Identify the blood parasite species.
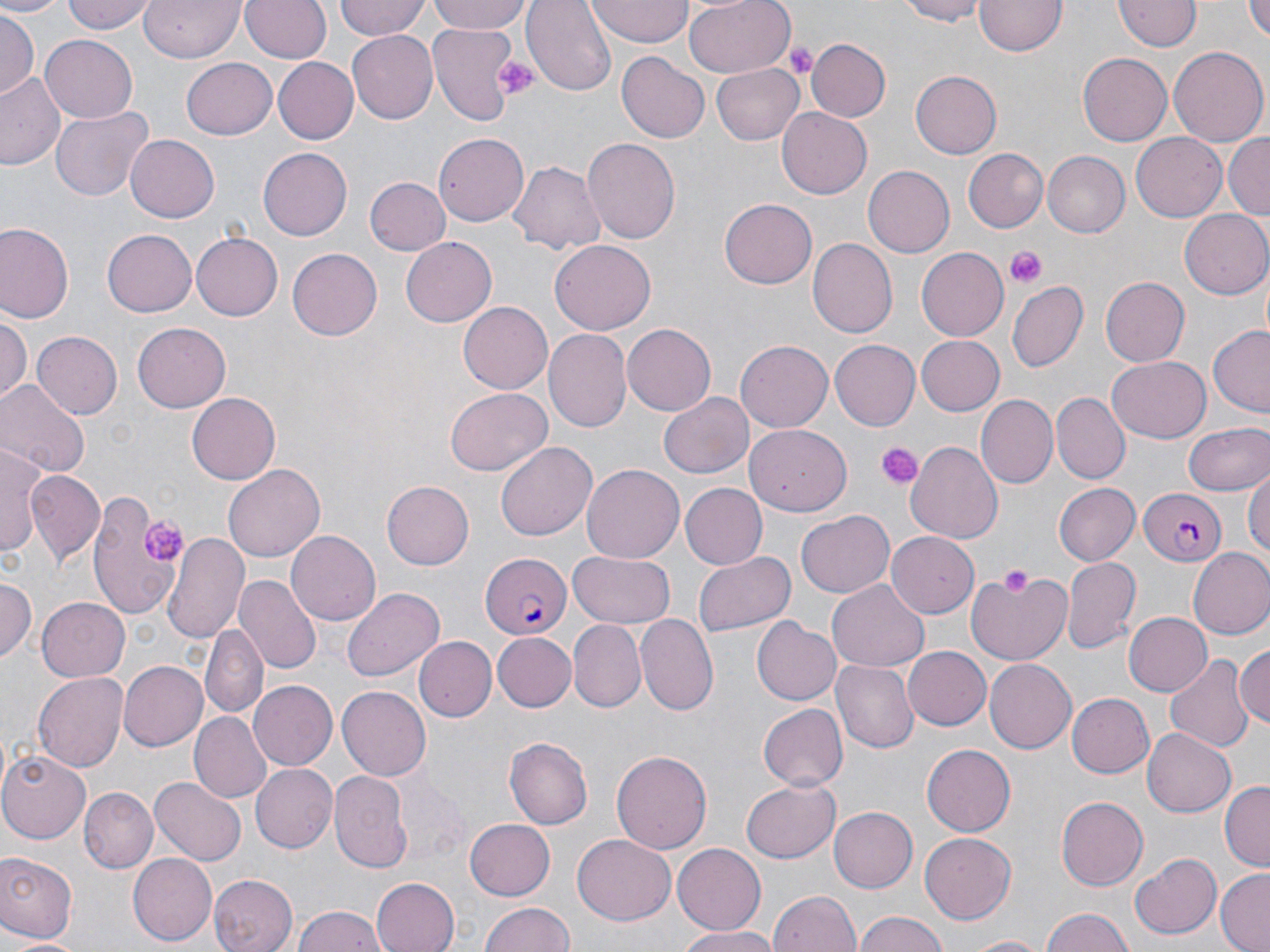

Plasmodium falciparum.

magnification = 1000x
Plasmodium falciparum-infected red blood cell locations = approximate bounding boxes as named x1/y1/x2/y2 corners in pixels: (x1=1137, y1=487, x2=1228, y2=567), (x1=481, y1=554, x2=571, y2=639)
uninfected red blood cell locations = approximate bounding boxes as named x1/y1/x2/y2 corners in pixels: (x1=0, y1=0, x2=61, y2=17), (x1=64, y1=0, x2=156, y2=35), (x1=137, y1=0, x2=246, y2=63), (x1=240, y1=0, x2=333, y2=63), (x1=333, y1=0, x2=431, y2=41), (x1=428, y1=0, x2=534, y2=36), (x1=523, y1=0, x2=617, y2=95), (x1=682, y1=0, x2=796, y2=78), (x1=893, y1=0, x2=992, y2=25), (x1=1117, y1=0, x2=1199, y2=52), (x1=975, y1=1, x2=1065, y2=56), (x1=587, y1=2, x2=697, y2=45), (x1=1245, y1=2, x2=1270, y2=44), (x1=0, y1=11, x2=37, y2=98), (x1=427, y1=21, x2=523, y2=127), (x1=346, y1=30, x2=438, y2=123), (x1=40, y1=33, x2=137, y2=119), (x1=805, y1=38, x2=891, y2=123), (x1=1171, y1=48, x2=1267, y2=145), (x1=616, y1=50, x2=710, y2=142), (x1=1078, y1=51, x2=1174, y2=146), (x1=272, y1=56, x2=359, y2=143), (x1=182, y1=58, x2=277, y2=139), (x1=710, y1=64, x2=805, y2=143), (x1=0, y1=71, x2=65, y2=171), (x1=911, y1=71, x2=1001, y2=158), (x1=50, y1=103, x2=152, y2=202), (x1=776, y1=107, x2=872, y2=199), (x1=435, y1=133, x2=528, y2=229), (x1=1130, y1=133, x2=1227, y2=222), (x1=1225, y1=133, x2=1270, y2=222), (x1=126, y1=135, x2=219, y2=222), (x1=580, y1=135, x2=679, y2=242), (x1=258, y1=148, x2=353, y2=239), (x1=963, y1=148, x2=1050, y2=232), (x1=1042, y1=152, x2=1130, y2=238), (x1=507, y1=160, x2=608, y2=257), (x1=864, y1=165, x2=954, y2=257), (x1=364, y1=175, x2=450, y2=257), (x1=720, y1=199, x2=816, y2=288), (x1=1181, y1=209, x2=1270, y2=298), (x1=0, y1=224, x2=75, y2=325), (x1=102, y1=228, x2=197, y2=317), (x1=192, y1=231, x2=283, y2=321), (x1=401, y1=237, x2=496, y2=327), (x1=549, y1=238, x2=656, y2=334), (x1=806, y1=238, x2=896, y2=337), (x1=915, y1=246, x2=1008, y2=341), (x1=288, y1=247, x2=385, y2=340), (x1=1101, y1=276, x2=1189, y2=367), (x1=1009, y1=280, x2=1087, y2=371), (x1=457, y1=302, x2=553, y2=395), (x1=0, y1=317, x2=29, y2=402), (x1=133, y1=321, x2=231, y2=413), (x1=621, y1=324, x2=716, y2=417), (x1=1208, y1=326, x2=1270, y2=415), (x1=544, y1=329, x2=631, y2=432), (x1=31, y1=332, x2=122, y2=420), (x1=914, y1=335, x2=1004, y2=415), (x1=737, y1=341, x2=832, y2=431), (x1=831, y1=341, x2=920, y2=430), (x1=1107, y1=357, x2=1212, y2=442), (x1=0, y1=380, x2=87, y2=481), (x1=445, y1=387, x2=552, y2=476), (x1=1051, y1=392, x2=1128, y2=484), (x1=186, y1=393, x2=279, y2=484), (x1=661, y1=393, x2=754, y2=478), (x1=977, y1=394, x2=1057, y2=488), (x1=746, y1=421, x2=851, y2=513), (x1=1183, y1=421, x2=1270, y2=497), (x1=495, y1=439, x2=596, y2=538), (x1=906, y1=440, x2=1003, y2=543), (x1=0, y1=442, x2=46, y2=558), (x1=225, y1=463, x2=325, y2=559), (x1=582, y1=464, x2=686, y2=563), (x1=1244, y1=468, x2=1270, y2=564), (x1=28, y1=470, x2=104, y2=564), (x1=382, y1=481, x2=474, y2=568), (x1=678, y1=482, x2=766, y2=569), (x1=1053, y1=484, x2=1141, y2=564), (x1=84, y1=490, x2=179, y2=620), (x1=796, y1=510, x2=895, y2=597), (x1=288, y1=529, x2=383, y2=626), (x1=887, y1=531, x2=979, y2=617), (x1=161, y1=532, x2=249, y2=644), (x1=1187, y1=548, x2=1270, y2=641), (x1=693, y1=549, x2=795, y2=639), (x1=566, y1=551, x2=678, y2=628), (x1=1061, y1=555, x2=1141, y2=653), (x1=965, y1=570, x2=1072, y2=666), (x1=234, y1=576, x2=321, y2=675), (x1=0, y1=577, x2=37, y2=663), (x1=829, y1=579, x2=930, y2=671), (x1=344, y1=587, x2=446, y2=682), (x1=38, y1=598, x2=130, y2=681), (x1=1124, y1=612, x2=1209, y2=695), (x1=634, y1=614, x2=717, y2=715), (x1=752, y1=619, x2=840, y2=706), (x1=570, y1=622, x2=645, y2=711), (x1=203, y1=625, x2=266, y2=722), (x1=493, y1=633, x2=576, y2=712), (x1=414, y1=637, x2=495, y2=722), (x1=1234, y1=644, x2=1269, y2=733), (x1=902, y1=645, x2=991, y2=729), (x1=1166, y1=654, x2=1250, y2=751), (x1=833, y1=658, x2=918, y2=752), (x1=985, y1=658, x2=1078, y2=753), (x1=118, y1=660, x2=209, y2=751), (x1=34, y1=672, x2=130, y2=772), (x1=248, y1=680, x2=337, y2=771), (x1=338, y1=686, x2=432, y2=781), (x1=1065, y1=692, x2=1155, y2=779), (x1=756, y1=703, x2=847, y2=791), (x1=188, y1=712, x2=272, y2=803), (x1=1142, y1=726, x2=1235, y2=816), (x1=504, y1=736, x2=594, y2=830), (x1=921, y1=743, x2=1016, y2=837), (x1=611, y1=749, x2=713, y2=857), (x1=0, y1=754, x2=91, y2=842), (x1=249, y1=763, x2=337, y2=852), (x1=329, y1=771, x2=412, y2=873), (x1=389, y1=772, x2=467, y2=862), (x1=151, y1=776, x2=245, y2=865), (x1=741, y1=780, x2=840, y2=863), (x1=1220, y1=782, x2=1270, y2=870), (x1=79, y1=788, x2=158, y2=873), (x1=1056, y1=795, x2=1148, y2=891), (x1=829, y1=806, x2=917, y2=893), (x1=465, y1=820, x2=557, y2=900), (x1=922, y1=832, x2=1018, y2=924), (x1=573, y1=835, x2=676, y2=923), (x1=673, y1=843, x2=765, y2=934), (x1=128, y1=852, x2=217, y2=944), (x1=1130, y1=852, x2=1222, y2=939), (x1=0, y1=853, x2=77, y2=942), (x1=1214, y1=869, x2=1270, y2=951), (x1=210, y1=873, x2=297, y2=952), (x1=370, y1=876, x2=458, y2=952), (x1=766, y1=889, x2=864, y2=952), (x1=480, y1=902, x2=575, y2=952), (x1=291, y1=907, x2=386, y2=952), (x1=1038, y1=908, x2=1138, y2=952), (x1=851, y1=911, x2=951, y2=952), (x1=675, y1=926, x2=782, y2=951), (x1=7, y1=934, x2=93, y2=951), (x1=962, y1=934, x2=1053, y2=951)
platelet locations = approximate bounding boxes as named x1/y1/x2/y2 corners in pixels: (x1=780, y1=38, x2=818, y2=78), (x1=495, y1=55, x2=539, y2=97), (x1=1005, y1=245, x2=1046, y2=285), (x1=876, y1=443, x2=920, y2=490), (x1=140, y1=518, x2=189, y2=565), (x1=1000, y1=561, x2=1034, y2=599)
stain = May-Grünwald-Giemsa
modality = light microscopy
image size = 1270×952 pixels
field of view = single
preparation = thin blood film